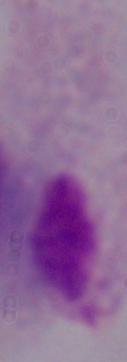

Micrograph. Captured at 1000x magnification. A trichomonad is shown.